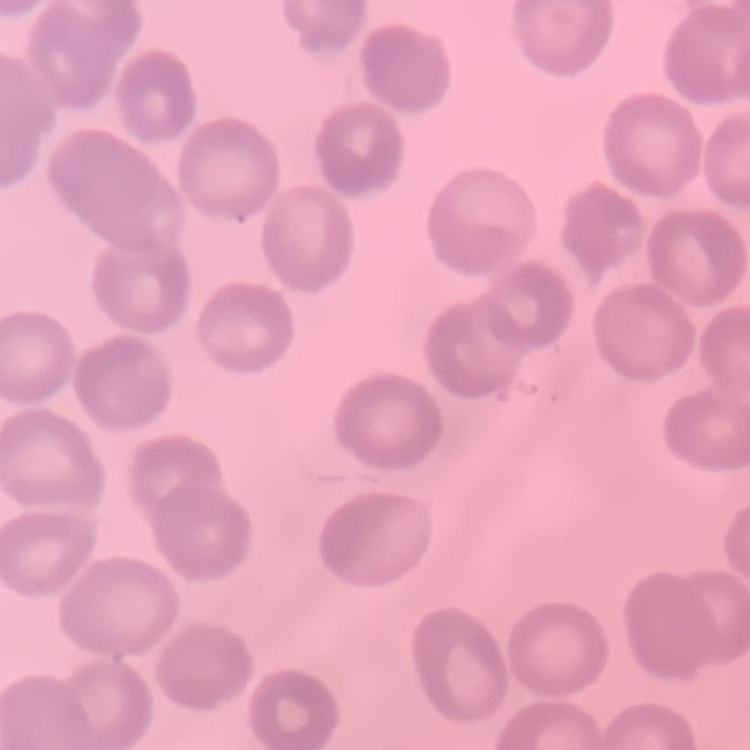
The erythrocytes show no rouleaux formation. Stained with either Field's or Giemsa. One tile cut from a larger photomicrograph. Thin blood smear.